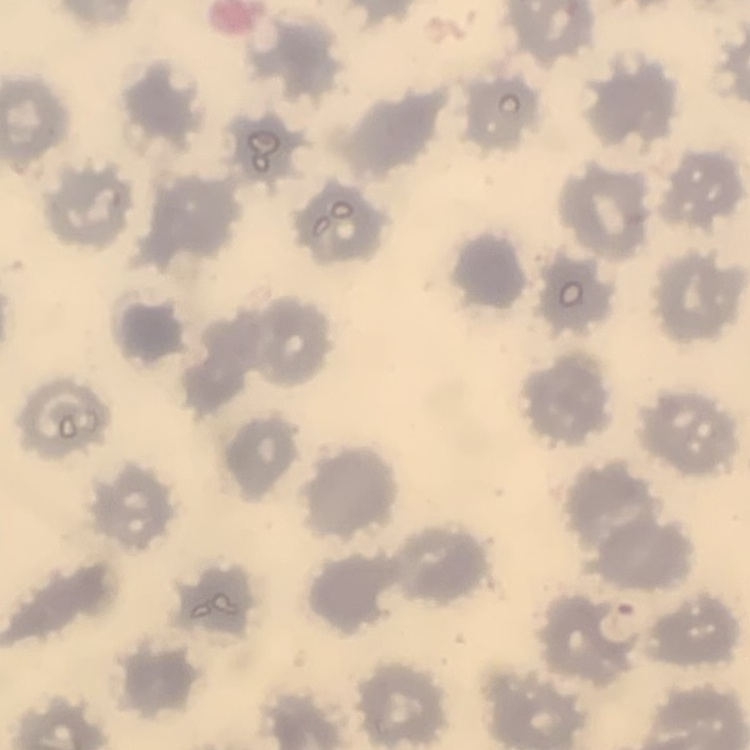

The erythrocytes exhibit no rouleaux formation. Thin peripheral smear. Stained with either Field's or Giemsa. One tile cut from a larger photomicrograph.